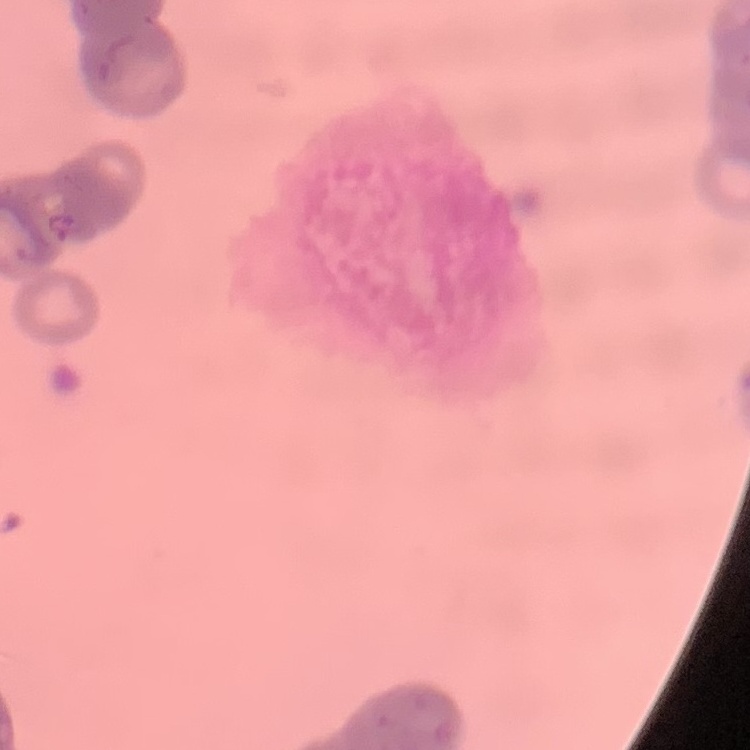 The red blood cells show rouleaux formation. Square crop of a larger photomicrograph. Thin blood film. Stained with either Field's or Giemsa.